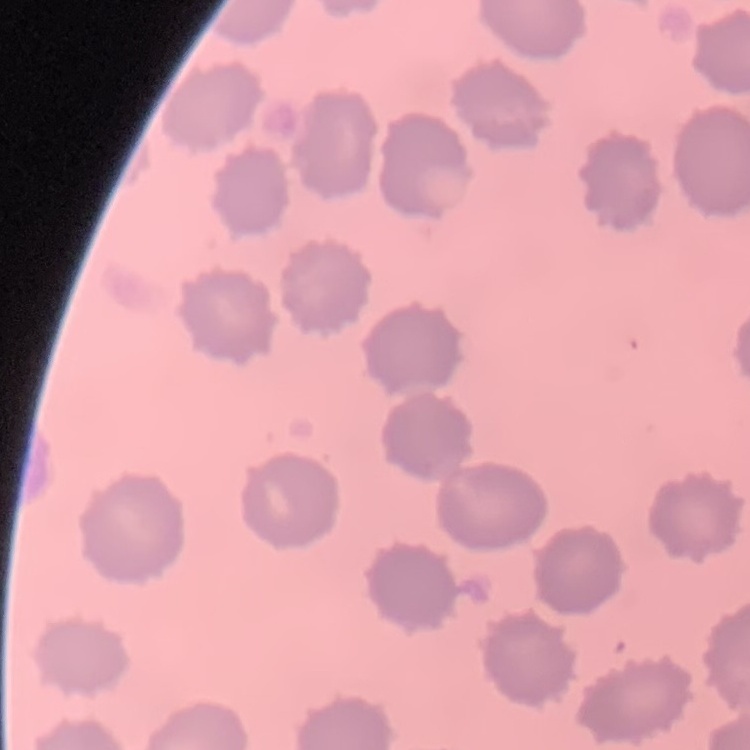
{
  "red_blood_cell_morphology": "no rouleaux formation",
  "image_type": "one tile cut from a larger photomicrograph",
  "preparation": "thin blood film",
  "stain": "Field's or Giemsa"
}